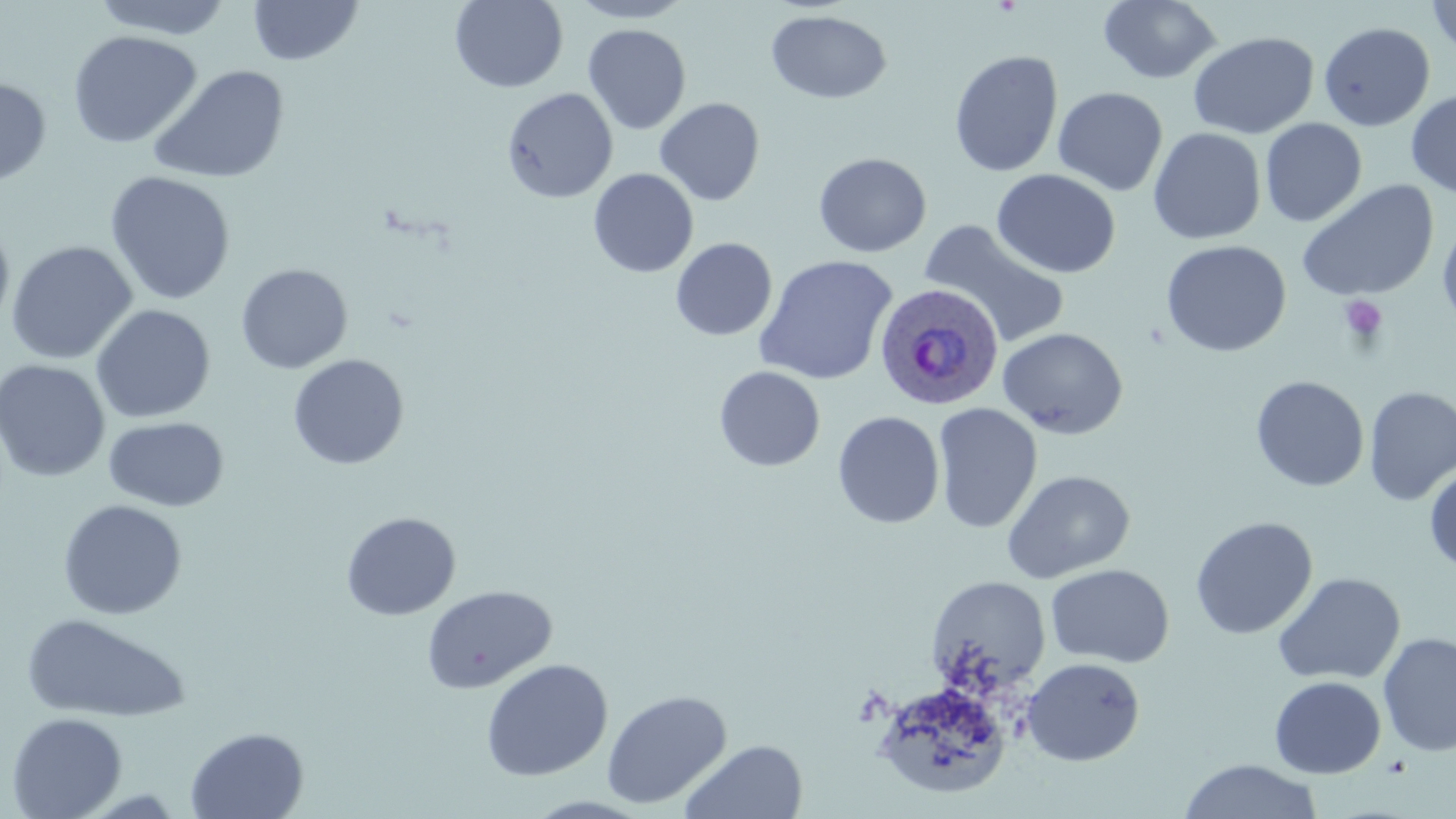

Summary:
  - Coordinate format: approximate bounding boxes as named x1/y1/x2/y2 corners in pixels
  - Plasmodium ovale-infected red blood cell locations: (x1=873, y1=283, x2=1004, y2=410)
  - Platelet locations: (x1=1339, y1=295, x2=1388, y2=343)
  - Uninfected red blood cell locations: (x1=91, y1=0, x2=235, y2=40), (x1=450, y1=0, x2=568, y2=94), (x1=566, y1=0, x2=697, y2=24), (x1=1098, y1=0, x2=1222, y2=84), (x1=1425, y1=0, x2=1456, y2=58), (x1=248, y1=1, x2=363, y2=66), (x1=766, y1=9, x2=892, y2=104), (x1=1318, y1=22, x2=1435, y2=131), (x1=583, y1=23, x2=691, y2=134), (x1=67, y1=30, x2=202, y2=149), (x1=1187, y1=31, x2=1320, y2=139), (x1=949, y1=50, x2=1064, y2=178), (x1=147, y1=64, x2=290, y2=185), (x1=0, y1=76, x2=52, y2=186), (x1=502, y1=87, x2=617, y2=203), (x1=1052, y1=87, x2=1168, y2=196), (x1=1406, y1=89, x2=1456, y2=197), (x1=654, y1=97, x2=765, y2=206), (x1=1260, y1=118, x2=1367, y2=227), (x1=1148, y1=127, x2=1266, y2=245), (x1=813, y1=152, x2=932, y2=257), (x1=588, y1=168, x2=699, y2=278), (x1=991, y1=168, x2=1121, y2=279), (x1=104, y1=171, x2=236, y2=305), (x1=1296, y1=180, x2=1439, y2=303), (x1=1437, y1=216, x2=1456, y2=335), (x1=0, y1=219, x2=15, y2=334), (x1=920, y1=219, x2=1071, y2=350), (x1=670, y1=237, x2=777, y2=341), (x1=6, y1=240, x2=138, y2=364), (x1=1160, y1=240, x2=1291, y2=358), (x1=754, y1=254, x2=898, y2=386), (x1=236, y1=263, x2=353, y2=374), (x1=90, y1=304, x2=216, y2=424), (x1=997, y1=327, x2=1128, y2=439), (x1=288, y1=354, x2=409, y2=470), (x1=0, y1=359, x2=110, y2=482), (x1=714, y1=365, x2=826, y2=472), (x1=1250, y1=375, x2=1369, y2=492), (x1=1364, y1=386, x2=1456, y2=506), (x1=932, y1=403, x2=1043, y2=533), (x1=832, y1=410, x2=945, y2=529), (x1=105, y1=416, x2=229, y2=512), (x1=1424, y1=462, x2=1456, y2=573), (x1=1002, y1=469, x2=1136, y2=584), (x1=58, y1=499, x2=188, y2=620), (x1=341, y1=512, x2=461, y2=621), (x1=1190, y1=516, x2=1318, y2=639), (x1=1045, y1=563, x2=1175, y2=668), (x1=1272, y1=572, x2=1406, y2=686), (x1=925, y1=576, x2=1051, y2=697), (x1=422, y1=585, x2=557, y2=694), (x1=21, y1=612, x2=192, y2=723), (x1=1377, y1=632, x2=1456, y2=757), (x1=1021, y1=657, x2=1146, y2=766), (x1=480, y1=659, x2=613, y2=781), (x1=1268, y1=675, x2=1386, y2=779), (x1=872, y1=680, x2=1013, y2=801), (x1=601, y1=689, x2=732, y2=810), (x1=6, y1=711, x2=128, y2=819), (x1=185, y1=726, x2=310, y2=819), (x1=679, y1=739, x2=808, y2=819), (x1=1178, y1=758, x2=1324, y2=818)
  - Slide-level diagnosis: Plasmodium ovale
  - Modality: optical microscopy
  - Field of view: one of a larger specimen
  - Magnification: 1000x
  - Image size: 1456×819 pixels
  - Stain: May-Grünwald-Giemsa
  - Preparation: thin blood smear